Assess this cell for malaria.
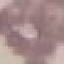

Uninfected.

Giemsa stain. Automatically extracted cell patch, resized to 64 × 64 pixels. Acquired by smartphone through the microscope eyepiece. Thin blood film.